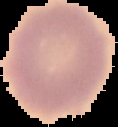
From a thin blood smear. Image is 118×127 pixels. Cell region segmented out of the field of view; the surrounding area is masked to black. Malaria status: uninfected.